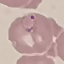
Result: malaria parasites identified. Giemsa stain. Cell patch, automatically extracted from a larger field of view and resized to 64 × 64 pixels. Thin blood smear. Acquired by smartphone through the microscope eyepiece.